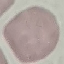
Malaria status: uninfected. Automatically extracted cell patch, resized to 64 × 64 pixels. Giemsa-stained preparation. Acquired by smartphone through the microscope eyepiece. Thin blood smear.